Point out leukocytes.
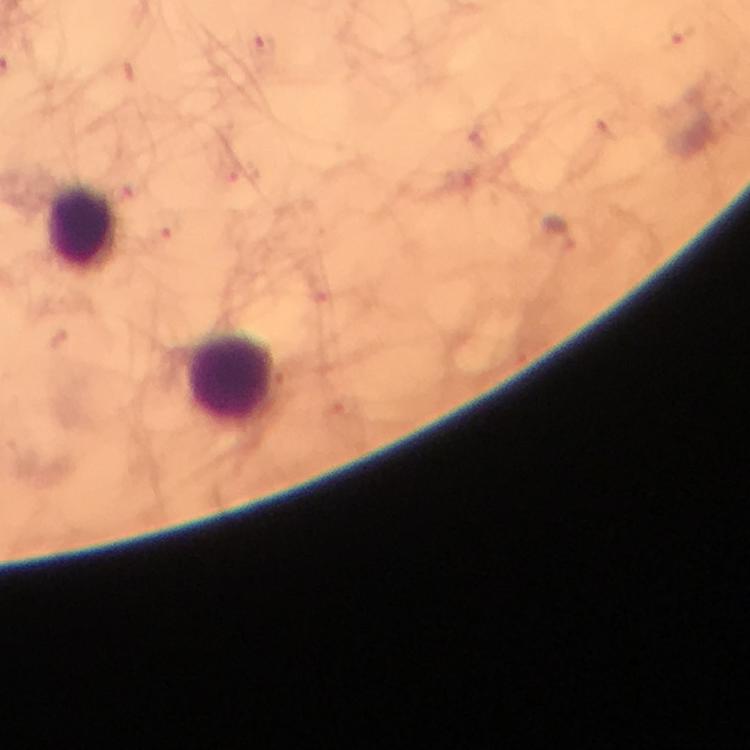
Approximate centers as {x, y} in pixels.
Leukocytes: {81, 230}, {233, 378}.

cropped from = a single field of view
preparation = thick smear
stain = Giemsa
context = from a diagnostic examination for malaria
Plasmodium parasites = none seen
magnification = 100x
image size = 750×750 pixels
immersion oil = used
capture = smartphone photograph through a microscope